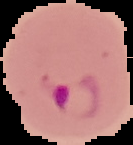
Summary:
  - Malaria status: parasitized
  - Preparation: thin blood smear
  - Image type: segmented cell region on a black background
  - Image size: 133×145 pixels